Outline each blood parasite and name the species.
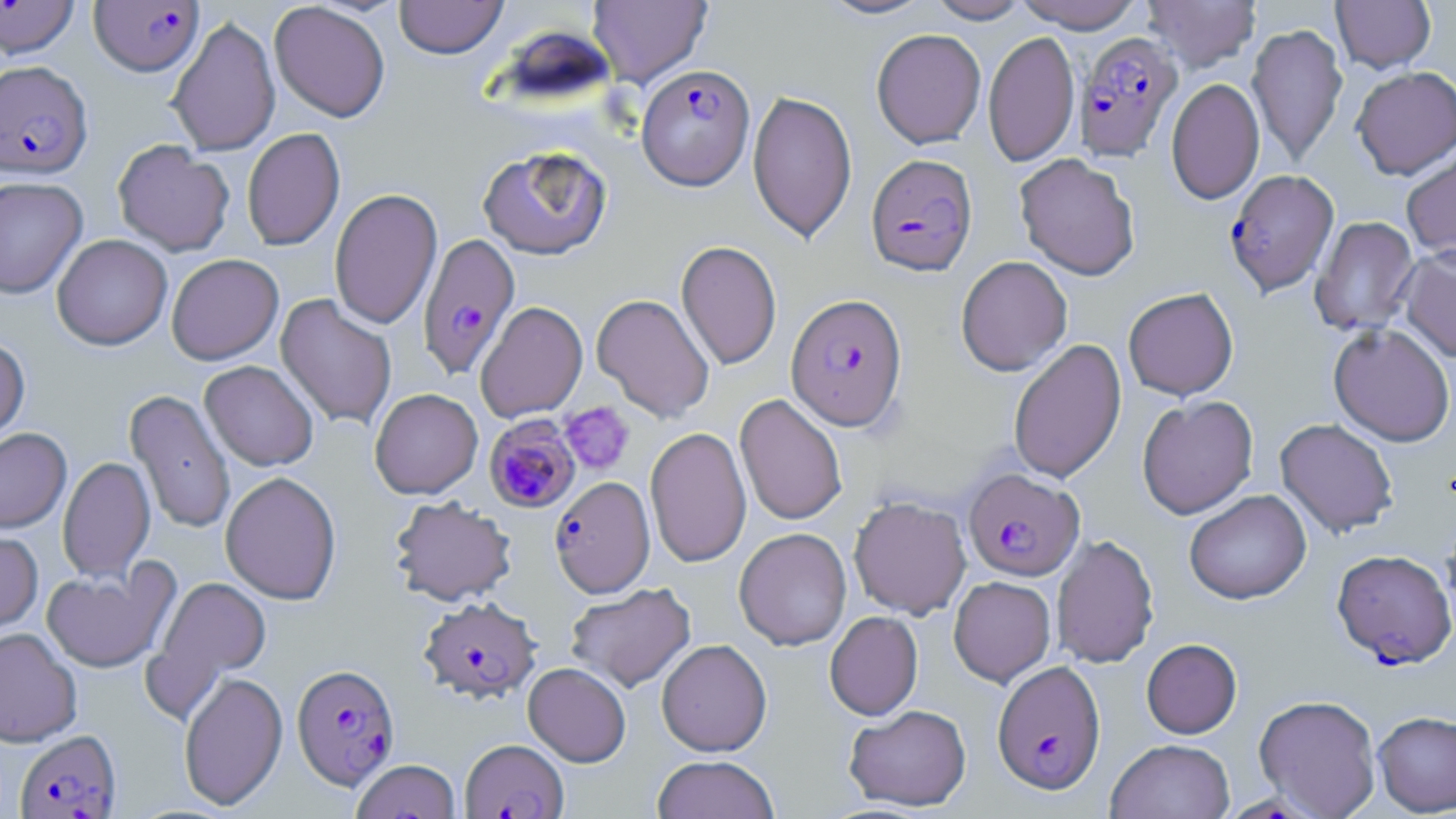
Approximate bounding boxes as [x1, y1, x2, y2] in pixels.
Plasmodium falciparum-infected red blood cells: [0, 1, 80, 59], [89, 1, 204, 76], [1074, 32, 1183, 162], [0, 60, 93, 179], [637, 63, 755, 190], [865, 153, 978, 277], [1224, 169, 1339, 297], [417, 233, 521, 380], [786, 293, 908, 431], [484, 417, 582, 514], [963, 468, 1084, 580], [549, 477, 655, 598], [1332, 550, 1455, 670], [418, 596, 541, 704], [992, 660, 1106, 794], [291, 663, 400, 790], [14, 729, 122, 819], [460, 739, 568, 818].
No Plasmodium ovale, Plasmodium malariae, Plasmodium vivax, Babesia divergens, or Trypanosoma brucei observed.

Summary:
  - Uninfected red blood cell locations: [395, 0, 508, 59], [588, 0, 712, 87], [817, 0, 936, 20], [926, 0, 1031, 24], [1011, 0, 1146, 32], [1142, 0, 1261, 73], [1331, 0, 1436, 74], [270, 2, 390, 122], [167, 15, 280, 156], [1247, 23, 1348, 168], [871, 28, 986, 149], [983, 29, 1080, 168], [1351, 66, 1456, 180], [1166, 78, 1264, 205], [747, 90, 857, 243], [242, 128, 345, 251], [112, 140, 234, 256], [477, 145, 612, 259], [1400, 146, 1456, 268], [1015, 153, 1140, 281], [0, 176, 88, 298], [329, 188, 443, 330], [1310, 216, 1420, 337], [52, 234, 172, 350], [676, 240, 782, 370], [1397, 246, 1456, 363], [166, 254, 283, 365], [956, 256, 1072, 376], [1122, 288, 1239, 400], [275, 293, 397, 431], [591, 294, 715, 423], [475, 301, 588, 423], [1328, 324, 1455, 447], [0, 336, 30, 448], [1008, 338, 1127, 484], [199, 360, 318, 471], [370, 388, 482, 499], [125, 389, 236, 534], [734, 394, 847, 526], [1137, 395, 1258, 519], [1275, 418, 1399, 538], [645, 426, 751, 568], [0, 428, 71, 533], [58, 456, 155, 583], [220, 471, 342, 605], [1184, 490, 1311, 604], [849, 495, 972, 619], [389, 496, 517, 606], [1439, 509, 1456, 633], [734, 528, 852, 650], [0, 530, 43, 635], [1051, 534, 1159, 668], [40, 561, 179, 674], [143, 574, 272, 715], [948, 576, 1056, 687], [565, 582, 696, 693], [824, 611, 923, 720], [0, 628, 82, 747], [1141, 638, 1242, 739], [657, 639, 772, 757], [523, 662, 631, 766], [179, 671, 288, 811], [1253, 694, 1382, 818], [844, 704, 972, 811], [1373, 711, 1456, 816], [1105, 739, 1235, 819], [651, 755, 780, 819], [351, 759, 460, 819]
  - Platelet locations: [558, 401, 635, 476]
  - Slide-level diagnosis: Plasmodium falciparum
  - Magnification: 1000x
  - Modality: optical microscopy
  - Preparation: thin blood smear
  - Field of view: one of a larger specimen
  - Image size: 1456×819 pixels
  - Stain: May-Grünwald-Giemsa